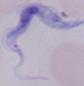
1000x magnification. Micrograph. A trypanosome is shown.